Outline every trophozoite.
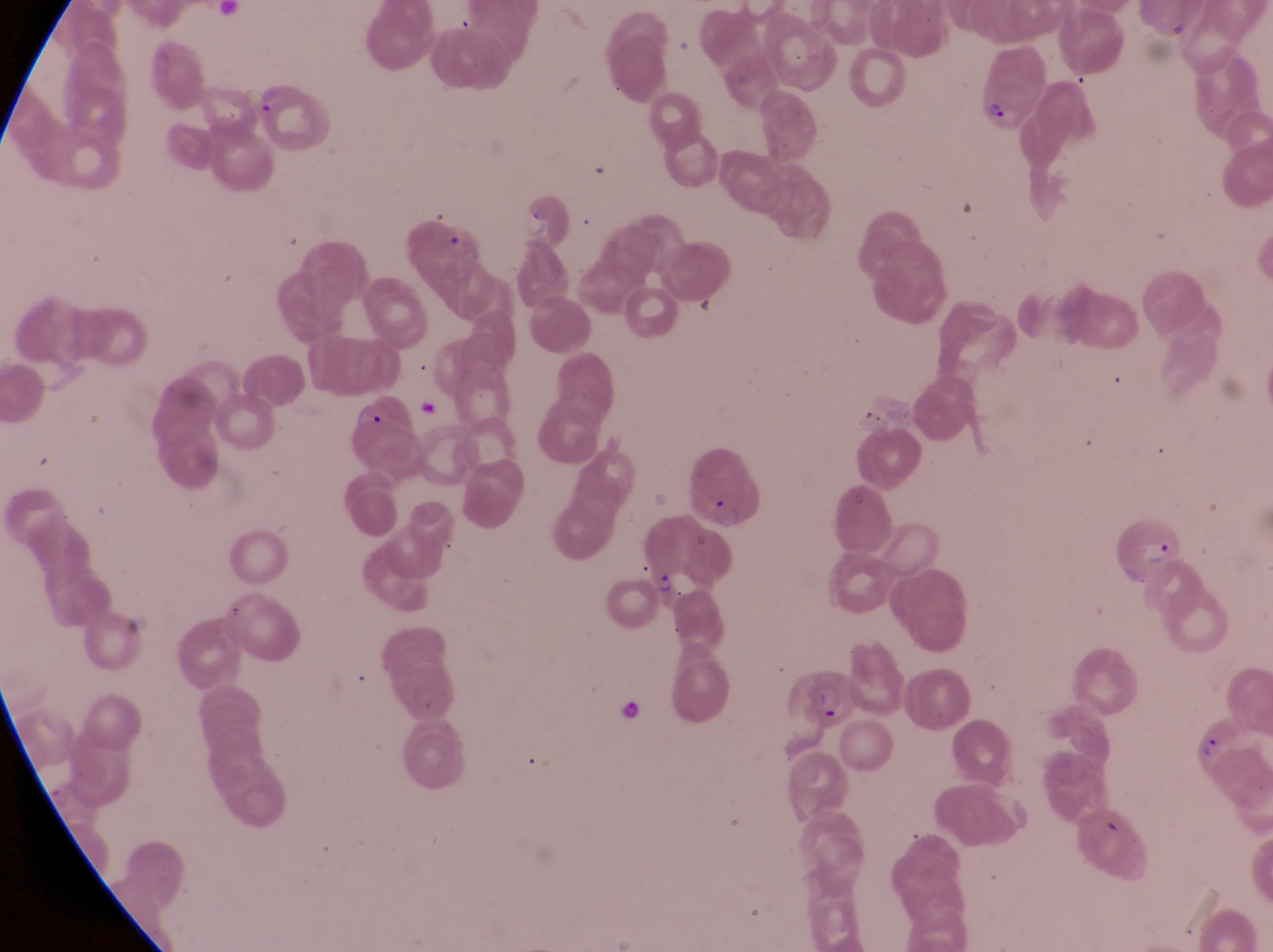

Approximate bounding boxes as {left, top, right, bottom} in pixels.
Trophozoites: {349, 400, 382, 427}, {1199, 732, 1231, 769}.

image_size: 1273×952 pixels
preparation: thin blood film
magnification: 1000x
country: Uganda
field_of_view: single
capture: smartphone photograph through the eyepiece of an Olympus CX-23 microscope
parasitised_red_blood_cell_locations: 'approximate bounding boxes as {left, top, right, bottom} in pixels: {248, 70, 328, 147}, {973, 70, 1036, 130}, {687, 444, 754, 534}, {1111, 507, 1180, 587}, {642, 552, 707, 604}, {792, 661, 857, 733}'